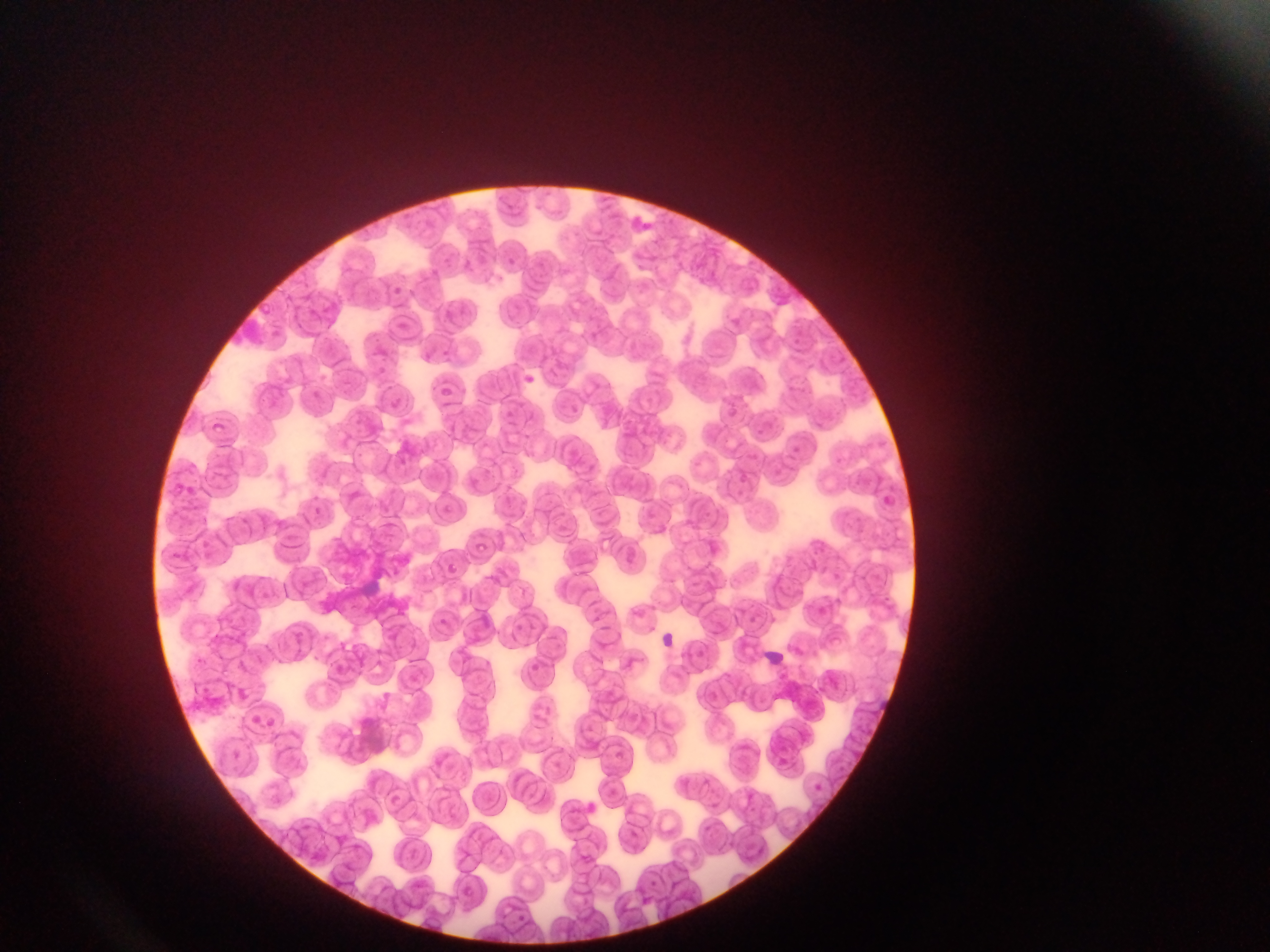
Approximate bounding boxes as {left, top, right, bottom} in pixels. Plasmodium parasite locations: {437, 383, 456, 394}, {212, 417, 235, 436}, {478, 540, 490, 553}. Image is 1270×952 pixels. Thin blood smear. Photographed through a microscope with a mobile-phone camera. Single field of view. Sample from Ghana.